Give the position of every Plasmodium parasite visible.
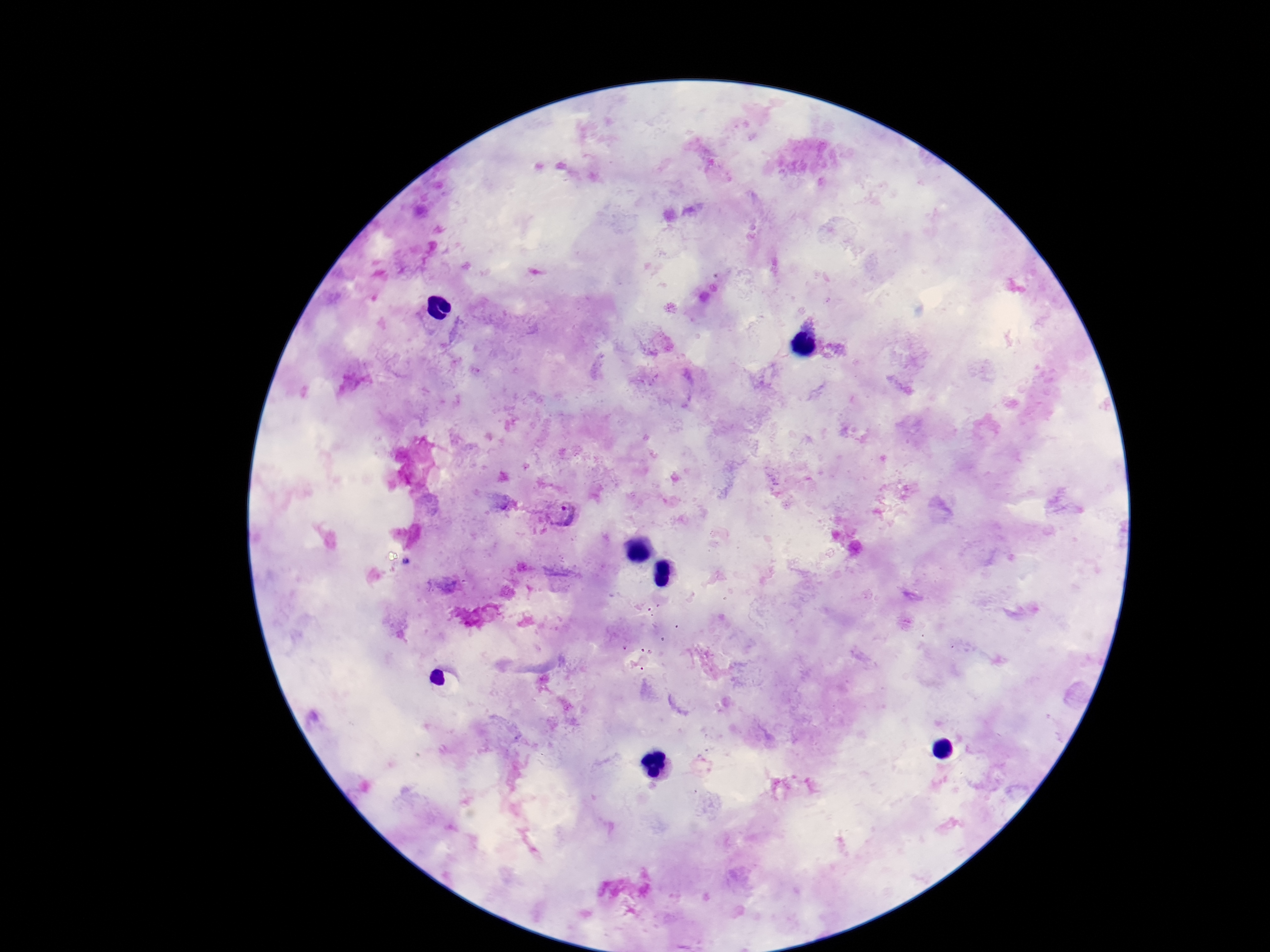

Approximate centers as {x, y} in pixels.
Plasmodium parasites: {561, 516}.

image size = 1270×952 pixels
patient malaria status = positive
magnification = 100x
field of view = single
stain = Giemsa
capture = smartphone camera through the microscope eyepiece
preparation = thick blood film